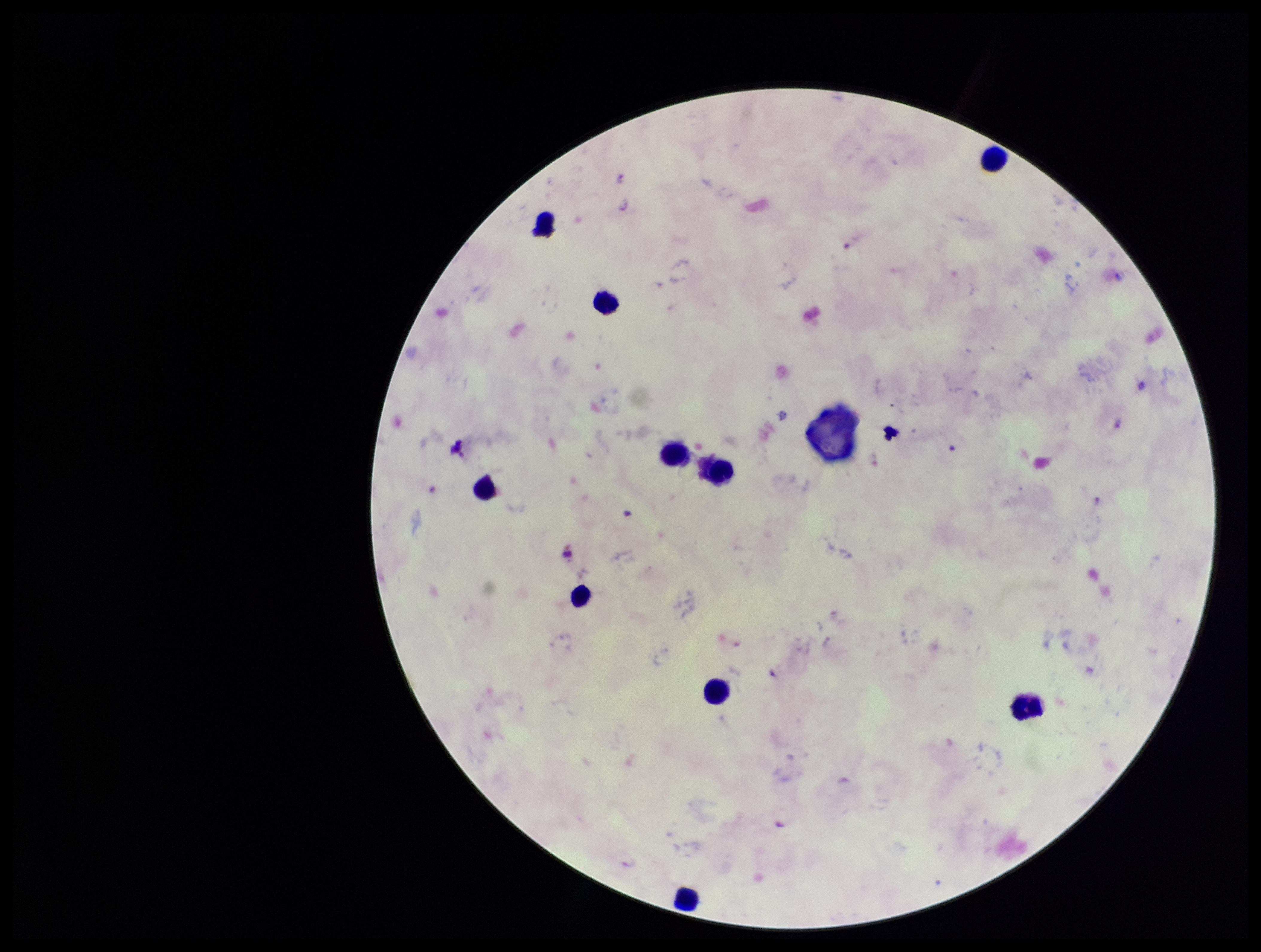

Summary:
  - Plasmodium parasites: none identified
  - Patient malaria status: infected
  - Preparation: thick smear
  - Image size: 1261×952 pixels
  - Leukocyte count: 10
  - Field of view: one from this slide
  - Capture: smartphone photograph through the microscope eyepiece
  - Stain: Giemsa
  - Parasite count: 0
  - Species reported for this patient: Plasmodium falciparum